Classify this cell by malaria status.
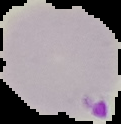
Parasitized.

{
  "image_size": "121×124 pixels",
  "image_type": "segmented cell region with the area outside set to black",
  "preparation": "thin blood film"
}